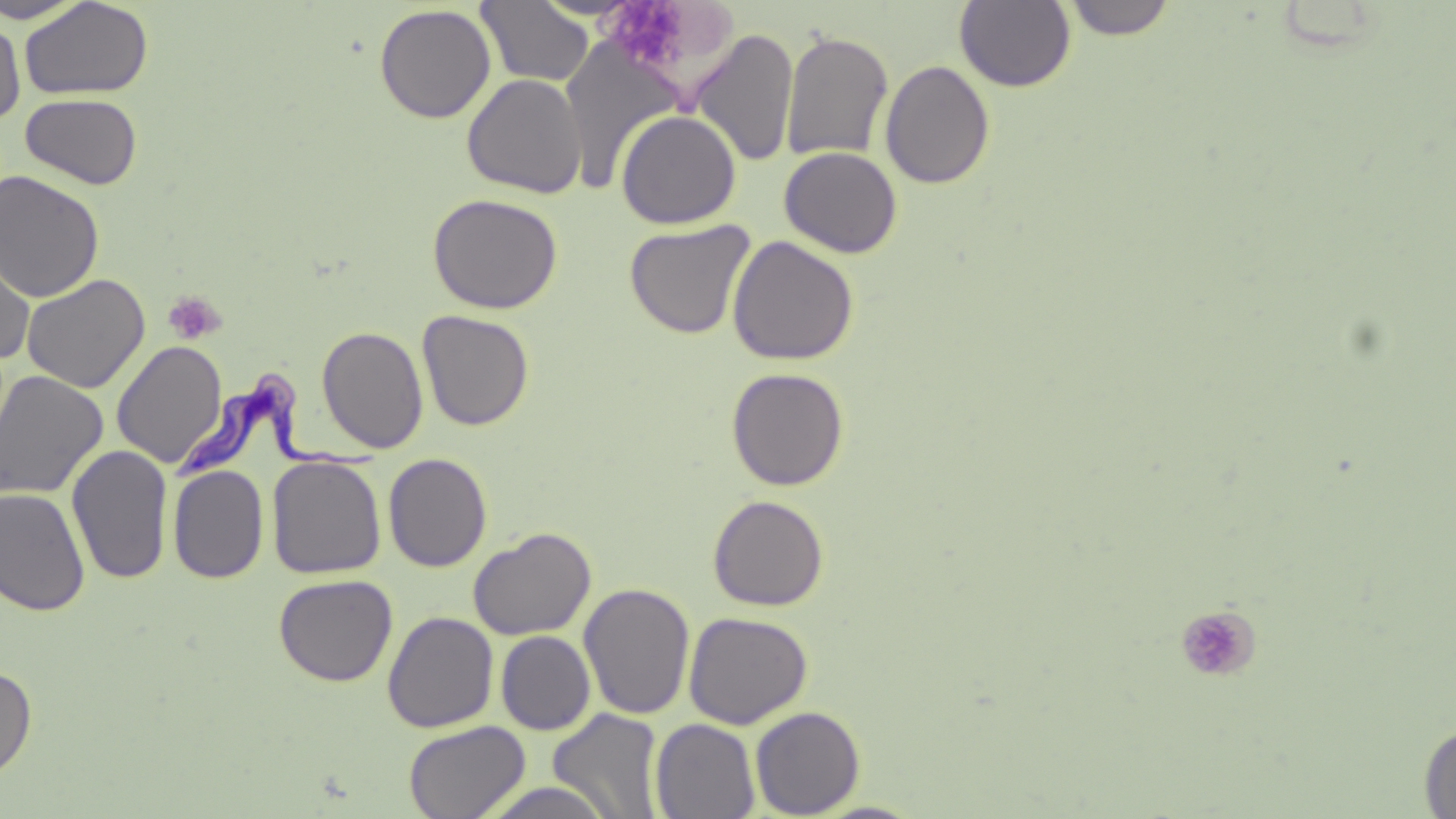 Approximate bounding boxes as (x1, y1, x2, y2) in pixels. Uninfected red blood cell locations: (475, 0, 595, 88), (1060, 0, 1179, 40), (0, 1, 90, 24), (20, 1, 154, 100), (954, 1, 1076, 92), (374, 4, 496, 123), (0, 15, 25, 125), (691, 28, 799, 167), (780, 29, 894, 163), (880, 60, 995, 189), (462, 73, 587, 198), (20, 93, 143, 189), (616, 109, 741, 229), (779, 146, 903, 258), (0, 169, 105, 302), (427, 193, 563, 314), (625, 219, 756, 340), (0, 232, 36, 364), (727, 235, 859, 366), (20, 273, 150, 393), (417, 309, 534, 431), (316, 325, 429, 453), (112, 340, 228, 468), (726, 367, 849, 491), (0, 370, 109, 501), (66, 444, 173, 585), (383, 452, 492, 572), (267, 456, 387, 579), (168, 464, 269, 584), (0, 488, 91, 616), (707, 494, 829, 611), (468, 527, 596, 641), (273, 573, 398, 686), (579, 582, 696, 721), (383, 611, 499, 733), (683, 611, 813, 729), (495, 631, 596, 735), (0, 664, 37, 781), (750, 706, 865, 818), (548, 708, 665, 818), (650, 718, 760, 819), (402, 720, 531, 819), (1418, 721, 1456, 817), (477, 781, 619, 818). Trypanosoma brucei locations: (168, 370, 382, 482). Platelet locations: (607, 0, 685, 67), (162, 291, 226, 344), (1175, 605, 1261, 683). Slide-level diagnosis: Trypanosoma brucei. May-Grünwald-Giemsa-stained preparation. One field of a larger specimen. Image is 1456×819 pixels. Optical microscopy. Thin blood smear. 1000x magnification.